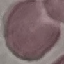

malaria status = uninfected
preparation = thin smear
image type = automatically extracted cell patch, resized to 64 × 64 pixels
capture = smartphone camera at the microscope eyepiece
stain = Giemsa